Give the extent of all white blood cells.
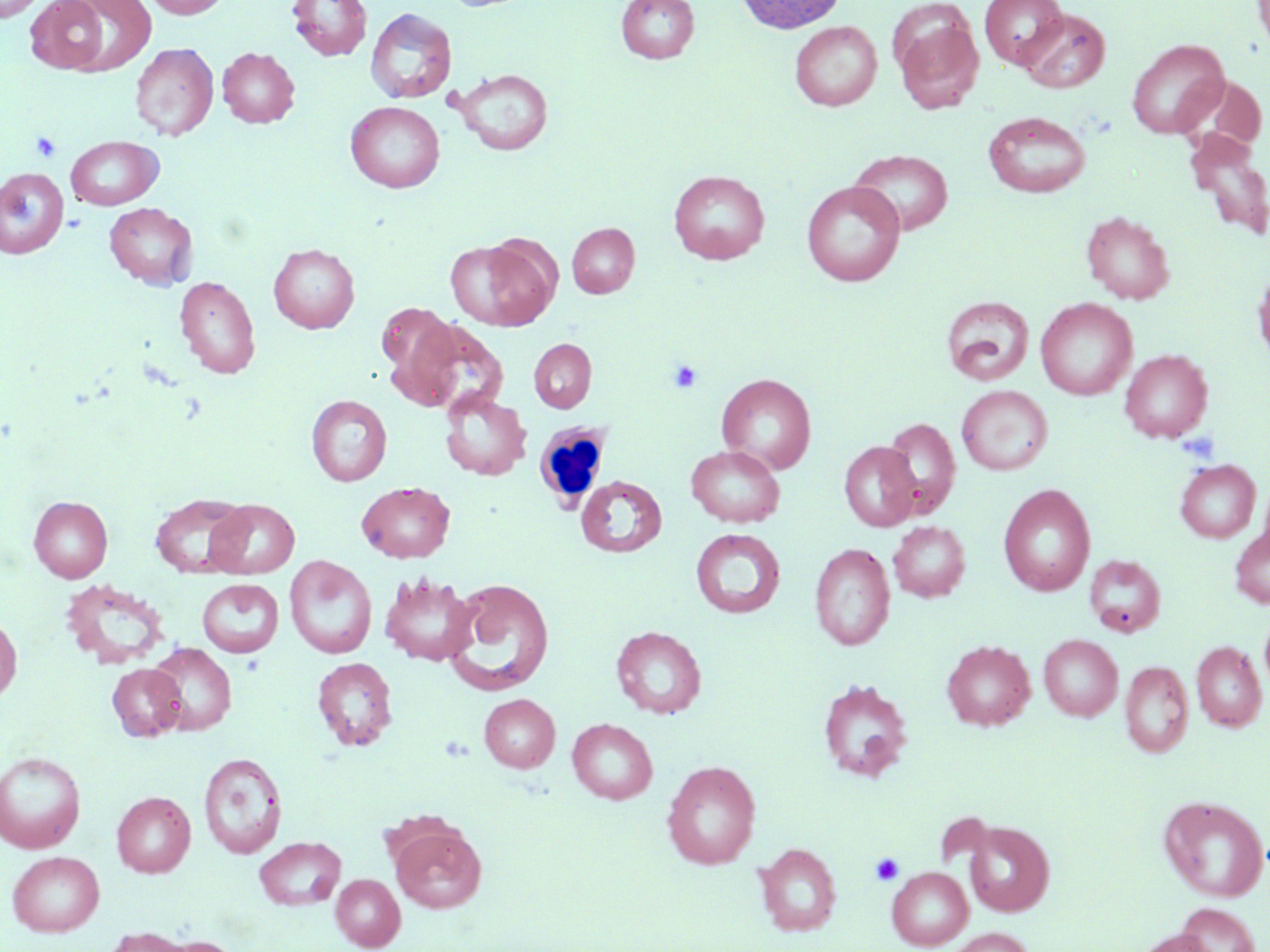

Approximate bounding boxes as (x1, y1, x2, y2) in pixels.
White blood cells: (532, 419, 612, 512).

Summary:
  - Uninfected red blood cell locations: (0, 0, 45, 23), (59, 0, 158, 77), (142, 0, 232, 18), (287, 0, 372, 61), (616, 0, 699, 64), (736, 0, 847, 34), (980, 0, 1068, 68), (1252, 0, 1270, 52), (26, 1, 112, 74), (366, 7, 457, 104), (1018, 8, 1110, 92), (893, 12, 984, 115), (790, 21, 882, 111), (1126, 38, 1230, 139), (130, 42, 218, 140), (218, 47, 300, 128), (455, 68, 553, 155), (1181, 74, 1267, 153), (345, 101, 444, 193), (983, 111, 1091, 197), (1188, 134, 1270, 239), (65, 135, 163, 210), (848, 149, 954, 236), (0, 167, 69, 258), (669, 170, 770, 264), (801, 181, 905, 286), (104, 202, 197, 290), (1081, 211, 1174, 304), (566, 222, 640, 298), (444, 239, 554, 330), (268, 243, 360, 333), (1253, 265, 1270, 366), (175, 276, 260, 380), (941, 296, 1034, 386), (1036, 298, 1137, 400), (378, 304, 460, 393), (405, 319, 507, 414), (529, 338, 596, 413), (1120, 350, 1212, 443), (717, 373, 817, 474), (957, 385, 1052, 475), (439, 389, 531, 480), (307, 395, 392, 486), (882, 418, 960, 516), (839, 441, 920, 532), (686, 444, 784, 528), (1175, 459, 1261, 542), (1259, 474, 1270, 557), (576, 475, 667, 558), (357, 481, 455, 562), (998, 484, 1096, 596), (150, 493, 252, 577), (29, 496, 112, 582), (207, 499, 300, 579), (889, 521, 970, 602), (1230, 525, 1270, 608), (690, 529, 786, 619), (809, 543, 894, 651), (1085, 554, 1166, 637), (284, 555, 377, 659), (380, 572, 478, 666), (444, 578, 554, 695), (197, 579, 283, 657), (1260, 611, 1270, 696), (0, 613, 22, 704), (610, 625, 706, 718), (1039, 634, 1122, 721), (942, 640, 1035, 730), (1192, 641, 1267, 732), (146, 642, 236, 735), (312, 656, 398, 751), (1120, 661, 1193, 758), (107, 663, 186, 741), (817, 678, 913, 781), (479, 694, 560, 772), (567, 718, 657, 804), (0, 751, 85, 853), (198, 753, 287, 859), (662, 760, 761, 869), (112, 791, 196, 877), (1159, 795, 1269, 902), (963, 820, 1055, 916), (388, 821, 487, 913), (254, 836, 346, 910), (754, 842, 842, 937), (7, 850, 104, 936), (886, 866, 973, 950), (331, 874, 405, 950), (1174, 903, 1261, 952), (942, 927, 1034, 952), (103, 928, 194, 952), (1134, 928, 1217, 952), (156, 935, 241, 952)
  - Platelet locations: (31, 131, 62, 162), (667, 359, 703, 393), (870, 853, 904, 885)
  - Slide-level diagnosis: no evidence of blood parasites
  - Stain: May-Grünwald-Giemsa
  - Preparation: thin blood film
  - Magnification: 1000x
  - Image size: 1270×952 pixels
  - Field of view: one of a larger specimen
  - Modality: optical microscopy